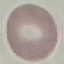

Summary:
  - Result: no malaria parasites detected
  - Image type: automatically extracted cell patch, resized to 64 × 64 pixels
  - Preparation: thin blood smear
  - Stain: Giemsa
  - Capture: smartphone through the microscope eyepiece